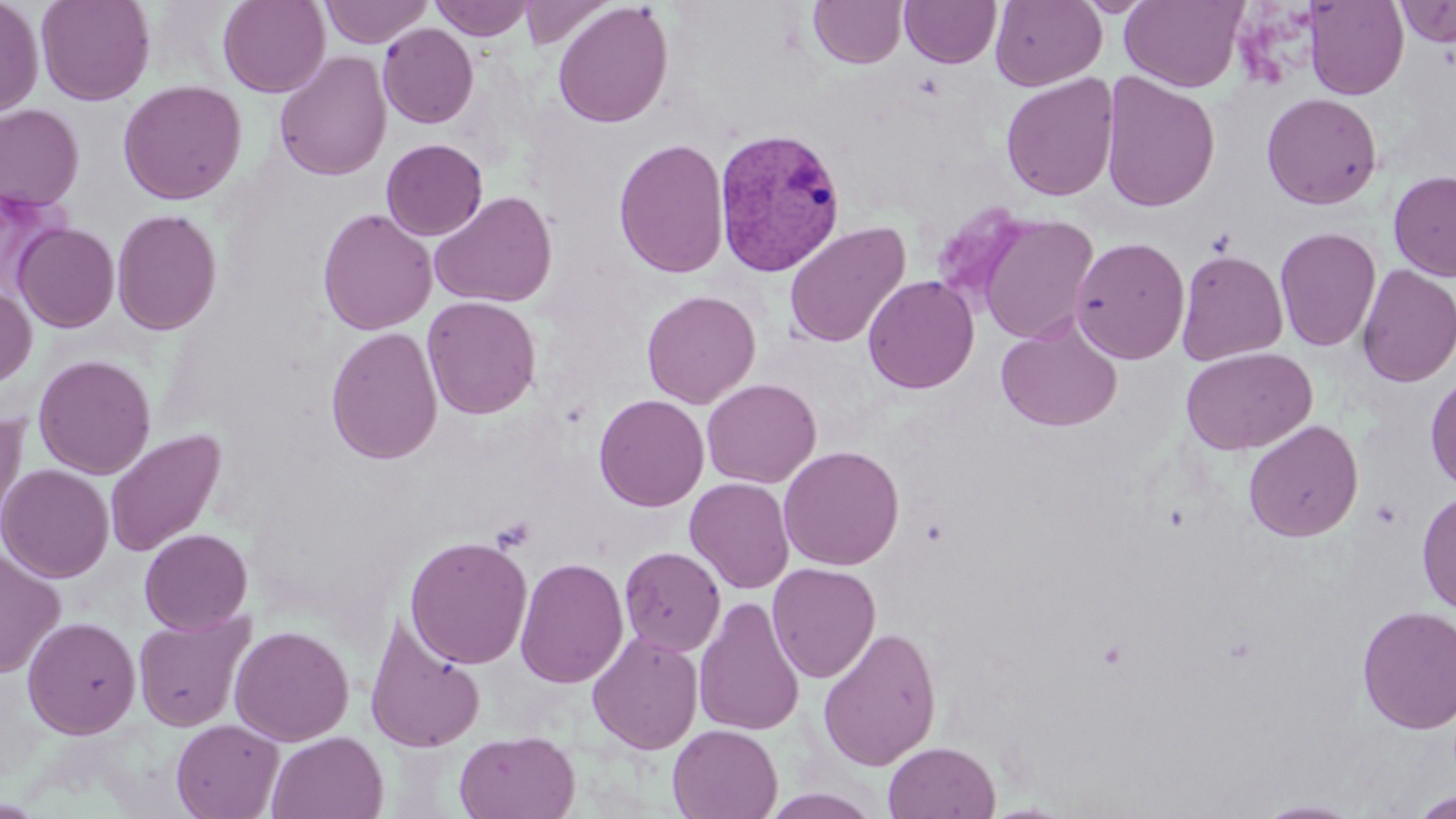
Approximate bounding boxes as [x1, y1, x2, y2] in pixels. Platelet locations: [491, 516, 536, 552]. Plasmodium vivax-infected red blood cell locations: [713, 127, 846, 277]. Uninfected red blood cell locations: [0, 0, 43, 117], [35, 0, 155, 106], [217, 0, 330, 97], [319, 0, 433, 47], [430, 0, 536, 40], [519, 0, 615, 49], [990, 0, 1107, 90], [1120, 0, 1248, 93], [808, 1, 908, 68], [899, 1, 1001, 68], [1303, 1, 1408, 100], [1394, 1, 1456, 47], [552, 2, 673, 128], [378, 23, 478, 128], [274, 51, 391, 181], [1100, 71, 1221, 212], [1001, 73, 1119, 202], [117, 80, 247, 205], [1261, 92, 1382, 210], [0, 104, 84, 211], [613, 137, 730, 279], [381, 138, 488, 240], [1388, 170, 1456, 282], [429, 191, 557, 308], [930, 202, 1033, 311], [111, 208, 222, 335], [317, 208, 436, 336], [975, 213, 1099, 346], [784, 221, 911, 348], [13, 223, 119, 332], [1274, 227, 1381, 352], [1071, 236, 1190, 364], [1176, 250, 1288, 364], [1356, 264, 1456, 388], [862, 275, 979, 394], [0, 283, 37, 388], [642, 290, 760, 408], [422, 296, 542, 419], [996, 319, 1122, 433], [325, 326, 443, 465], [1181, 347, 1317, 455], [33, 354, 156, 479], [1425, 371, 1456, 493], [702, 378, 821, 488], [594, 394, 709, 511], [0, 414, 28, 538], [1243, 420, 1364, 542], [104, 428, 227, 558], [778, 445, 904, 571], [0, 463, 113, 583], [684, 477, 795, 594], [1417, 489, 1456, 616], [139, 528, 253, 635], [404, 535, 533, 669], [0, 546, 65, 679], [619, 546, 726, 657], [514, 556, 629, 689], [767, 562, 881, 683], [694, 596, 806, 737], [1357, 605, 1456, 734], [133, 609, 254, 732], [364, 614, 486, 753], [22, 616, 141, 739], [229, 625, 353, 746], [818, 626, 942, 771], [587, 631, 704, 755], [171, 719, 283, 819], [667, 724, 783, 819], [453, 729, 580, 818], [266, 730, 388, 819], [883, 741, 1001, 819], [761, 788, 883, 819], [1411, 789, 1456, 818], [1253, 799, 1367, 818]. Slide-level diagnosis: Plasmodium vivax. 1000x magnification. Thin blood smear. Image is 1456×819 pixels. May-Grünwald-Giemsa stain. Optical microscopy. One field of a larger specimen.